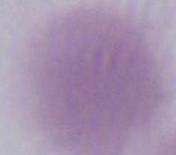

modality = photomicrograph
identification = erythrocyte
magnification = 1000x